Classify this cell by malaria status.
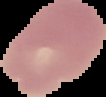

It is uninfected.

Cell region segmented out of the field of view; the surrounding area is masked to black. From a thin blood film. Image is 106×97 pixels.